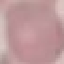
Malaria status: uninfected. Acquired by smartphone through the microscope eyepiece. Giemsa-stained preparation. Thin smear of blood. Automatically extracted cell patch, resized to 64 × 64 pixels.